State which parasite is depicted.
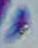
This is Toxoplasma gondii.

modality = micrograph
magnification = 1000x